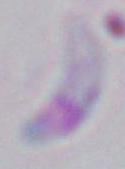 Micrograph. Toxoplasma gondii is seen. Captured at 1000x magnification.